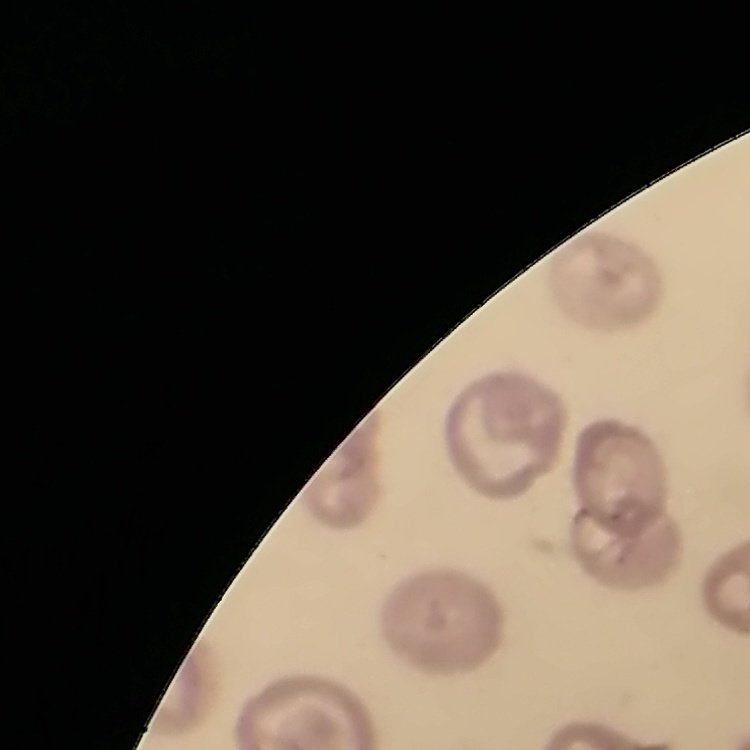

erythrocyte morphology = no rouleaux formation
stain = Field's or Giemsa
preparation = thin blood film
image type = one tile cut from a larger photomicrograph